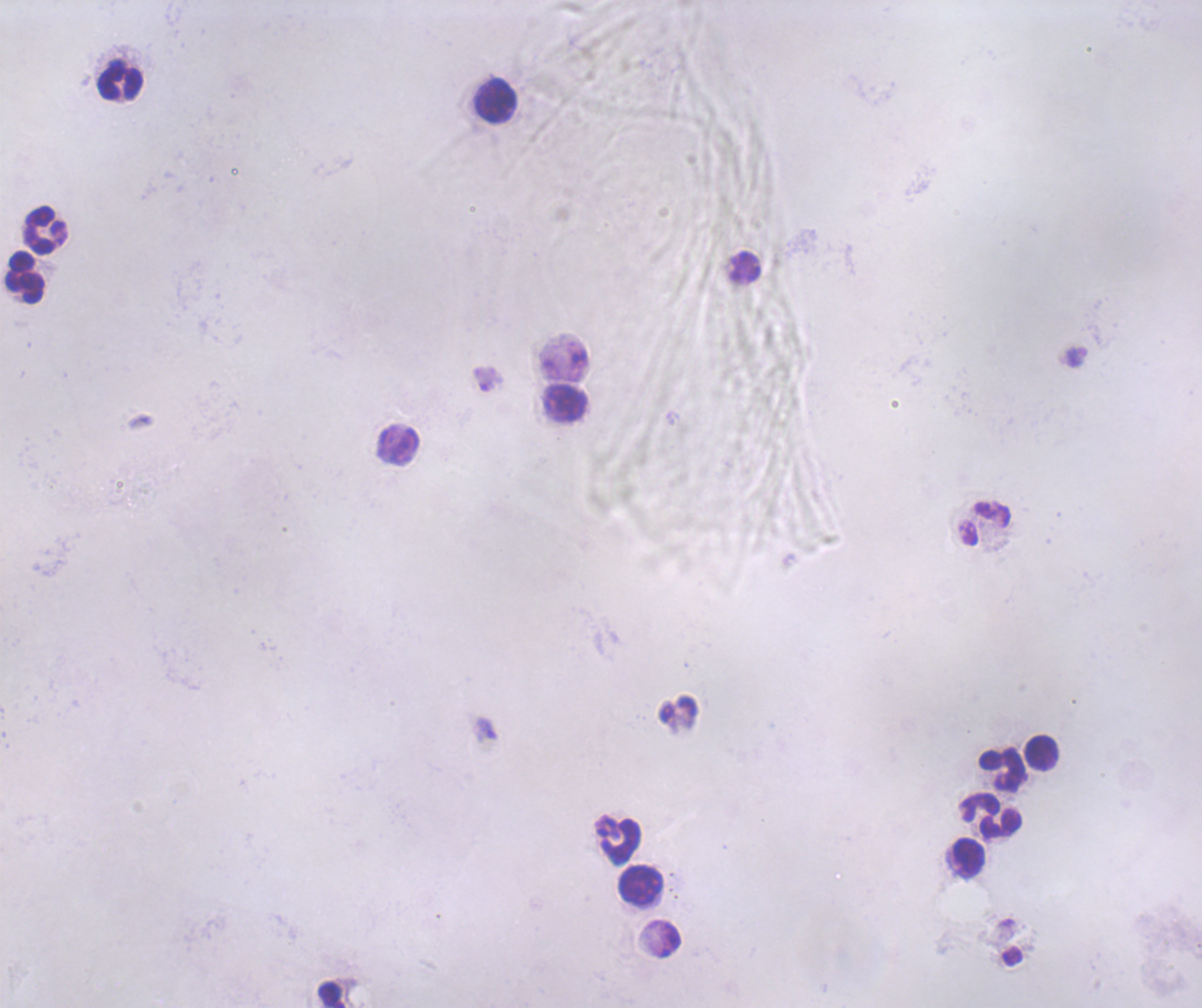
coordinate format = approximate centers as {x, y} in pixels
leukocyte locations = {120, 82}, {495, 101}, {46, 230}, {26, 278}, {565, 403}, {985, 524}, {1042, 752}, {1002, 770}, {990, 816}, {620, 842}, {969, 858}, {640, 884}, {331, 995}
trophozoite locations = {486, 730}
field of view = one from this slide
preparation = thick blood smear
context = previously used in a real diagnosis
coloration quality = bad
image size = 1202×1008 pixels
result = positive for malaria parasites
magnification = 100x
background quality = poor
stain = Romanowsky